Name the parasite shown.
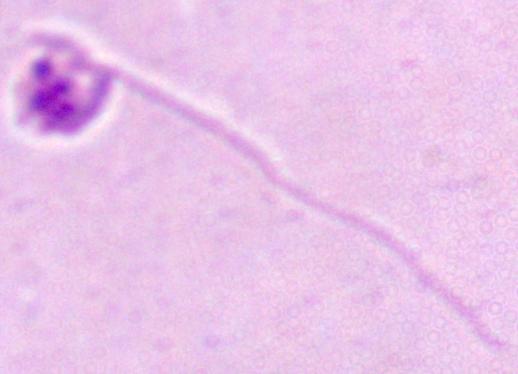

Leishmania.

Micrograph. 1000x magnification.